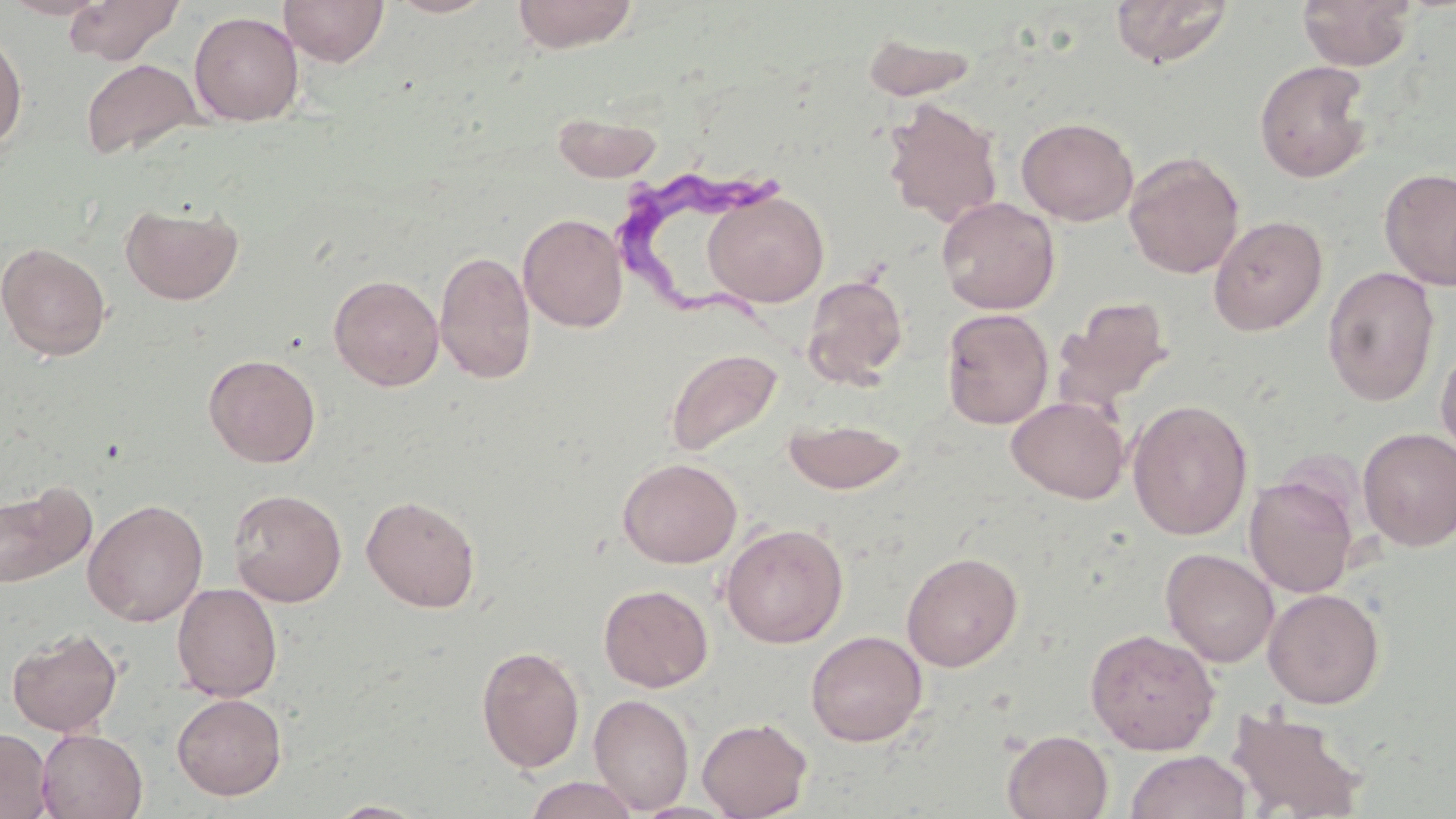
Approximate bounding boxes as (x1,y1)-(x2,y2) corner pairs in pixels. Trypanosoma brucei locations: (613,168)-(787,342). Uninfected red blood cell locations: (1,0)-(113,20), (63,0)-(184,65), (278,0)-(389,67), (385,0)-(497,18), (511,0)-(640,52), (1109,0)-(1234,68), (1297,0)-(1417,71), (189,11)-(304,126), (0,29)-(28,151), (860,30)-(981,102), (80,58)-(204,161), (1254,60)-(1374,183), (882,98)-(1004,227), (552,109)-(662,183), (1016,116)-(1139,226), (1123,151)-(1245,279), (1378,168)-(1456,290), (704,190)-(829,306), (936,197)-(1060,315), (120,201)-(243,305), (518,212)-(629,333), (1208,215)-(1328,335), (0,242)-(112,361), (434,249)-(536,384), (1322,266)-(1441,405), (329,274)-(444,391), (802,274)-(908,387), (1053,296)-(1174,412), (942,306)-(1179,422), (941,308)-(1054,429), (1435,340)-(1455,463), (665,347)-(783,458), (204,353)-(321,467), (1007,396)-(1129,503), (1127,399)-(1253,540), (783,417)-(908,495), (1357,427)-(1456,551), (617,457)-(742,567), (1244,474)-(1359,598), (0,480)-(96,590), (228,488)-(347,607), (361,494)-(481,612), (83,498)-(208,626), (720,522)-(849,648), (1161,548)-(1279,667), (901,551)-(1023,672), (172,582)-(282,702), (598,584)-(713,692), (1263,588)-(1384,709), (1084,626)-(1220,755), (6,627)-(123,737), (805,630)-(928,747), (476,645)-(586,773), (171,693)-(287,800), (588,694)-(694,814), (1225,704)-(1370,818), (696,716)-(812,819), (0,728)-(53,819), (37,729)-(149,819), (1002,729)-(1114,819), (1126,750)-(1251,819), (522,775)-(642,819), (326,800)-(431,818). Slide-level diagnosis: Trypanosoma brucei. One field of a larger specimen. May-Grünwald-Giemsa-stained preparation. Optical microscopy. Thin blood film. Image is 1456×819 pixels. Captured at 1000x magnification.